State which parasite is depicted.
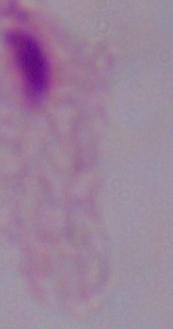
A trichomonad.

magnification = 1000x
modality = photomicrograph